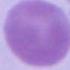

An erythrocyte is shown. Micrograph. Captured at 1000x magnification.